Comment on the morphology of the red blood cells.
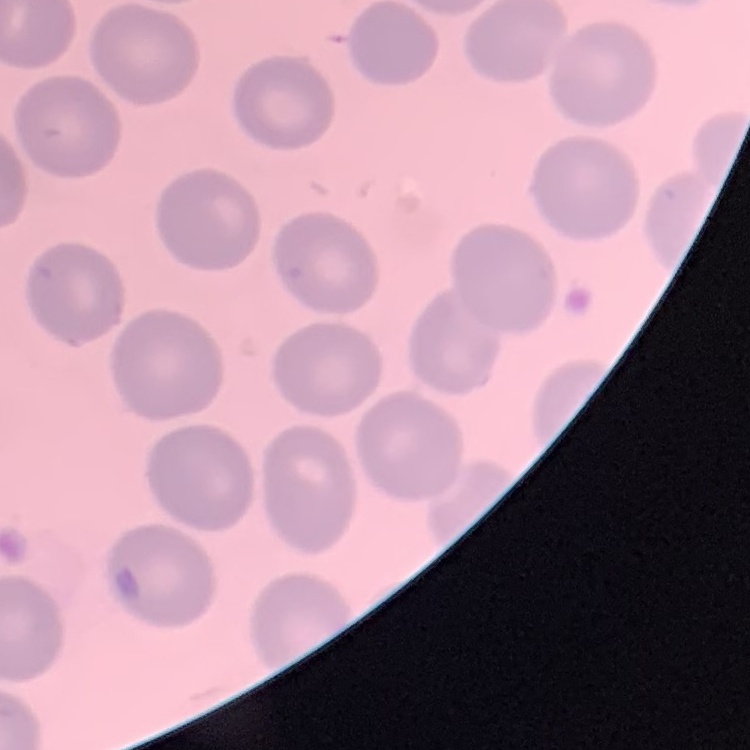

No rouleaux formation.

One tile cut from a larger photomicrograph. Thin peripheral smear. Field's or Giemsa stain.